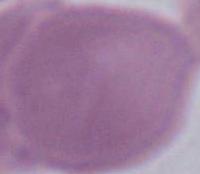

modality = micrograph
identification = red blood cell
magnification = 1000x